Assess for Plasmodium parasites.
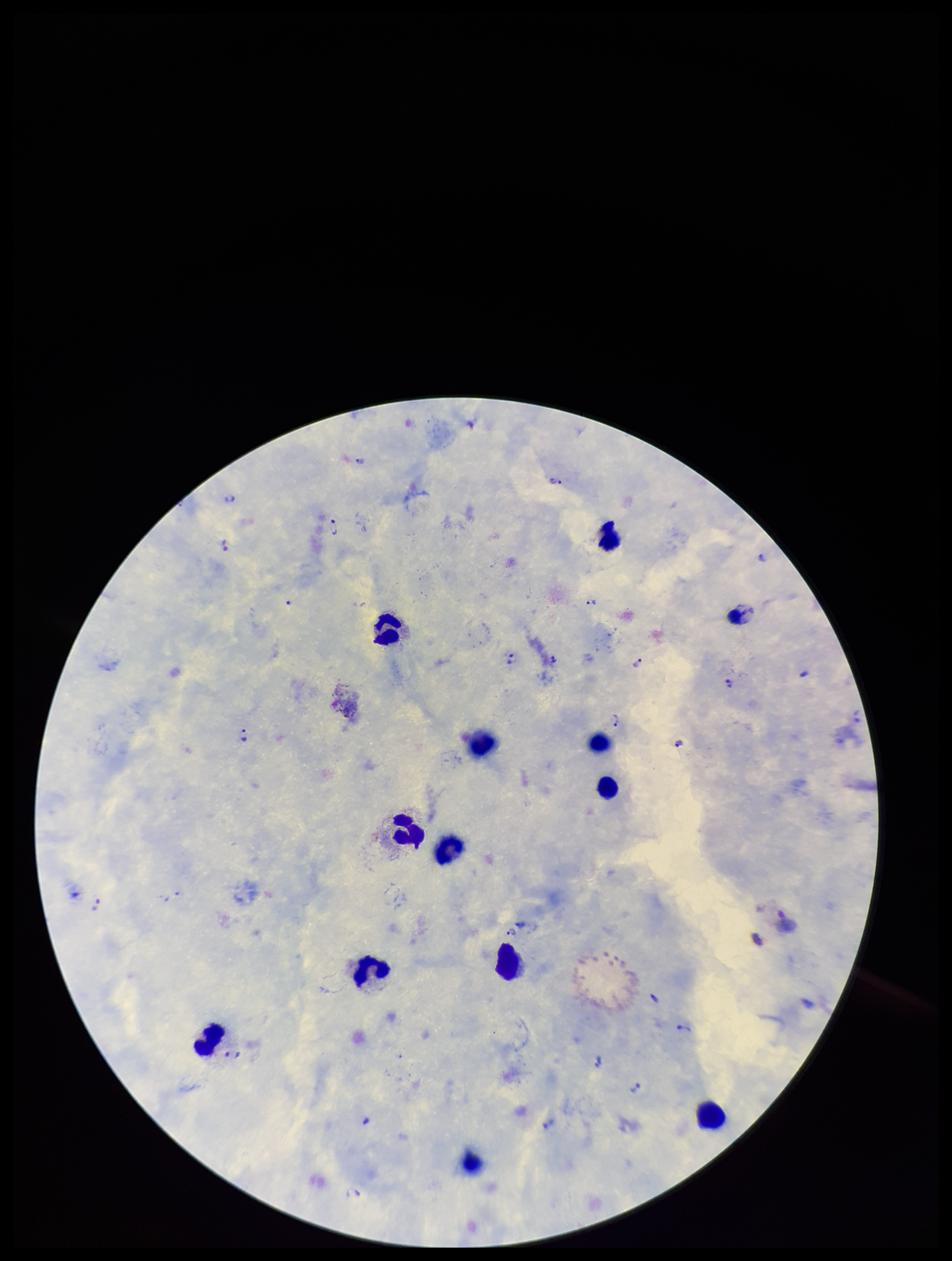

Detected.

image size = 952×1261 pixels
capture = smartphone photograph through the microscope eyepiece
field of view = single
species reported for this patient = Plasmodium vivax
preparation = thick blood smear
parasite count = 20
leukocyte count = 13
patient malaria status = positive
stain = Giemsa